Classify this cell by malaria status.
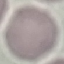

It is uninfected.

stain = Giemsa
capture = smartphone through the microscope eyepiece
image type = cell patch, automatically extracted from a larger field of view and resized to 64 × 64 pixels
preparation = thin blood smear